Assess this cell for malaria.
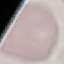

Uninfected.

Summary:
  - Preparation: thin smear
  - Capture: smartphone through the microscope eyepiece
  - Image type: cell patch, automatically extracted from a larger field of view and resized to 64 × 64 pixels
  - Stain: Giemsa